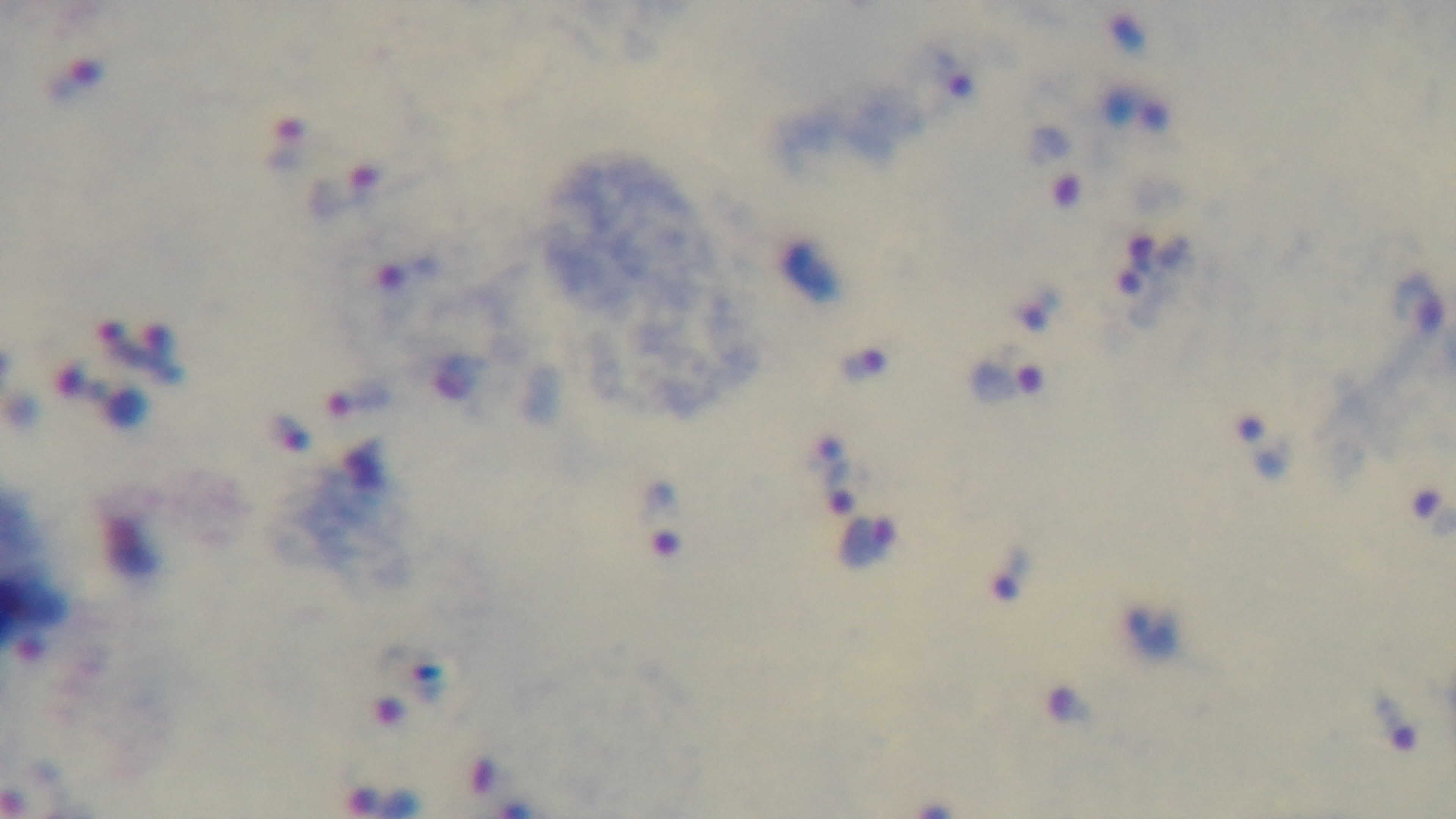

capture = mounted 4K digital camera
modality = light microscopy
preparation = thick smear
objective = 100x oil immersion
malaria status = infected
stain = Giemsa
field of view = one from the slide